Assess this cell for malaria.
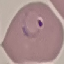

It is parasitized.

Thin blood film. Cell patch, automatically extracted from a larger field of view and resized to 64 × 64 pixels. Giemsa-stained preparation. Photographed with a smartphone camera at the microscope eyepiece.